Outline each Plasmodium vivax-infected red blood cell.
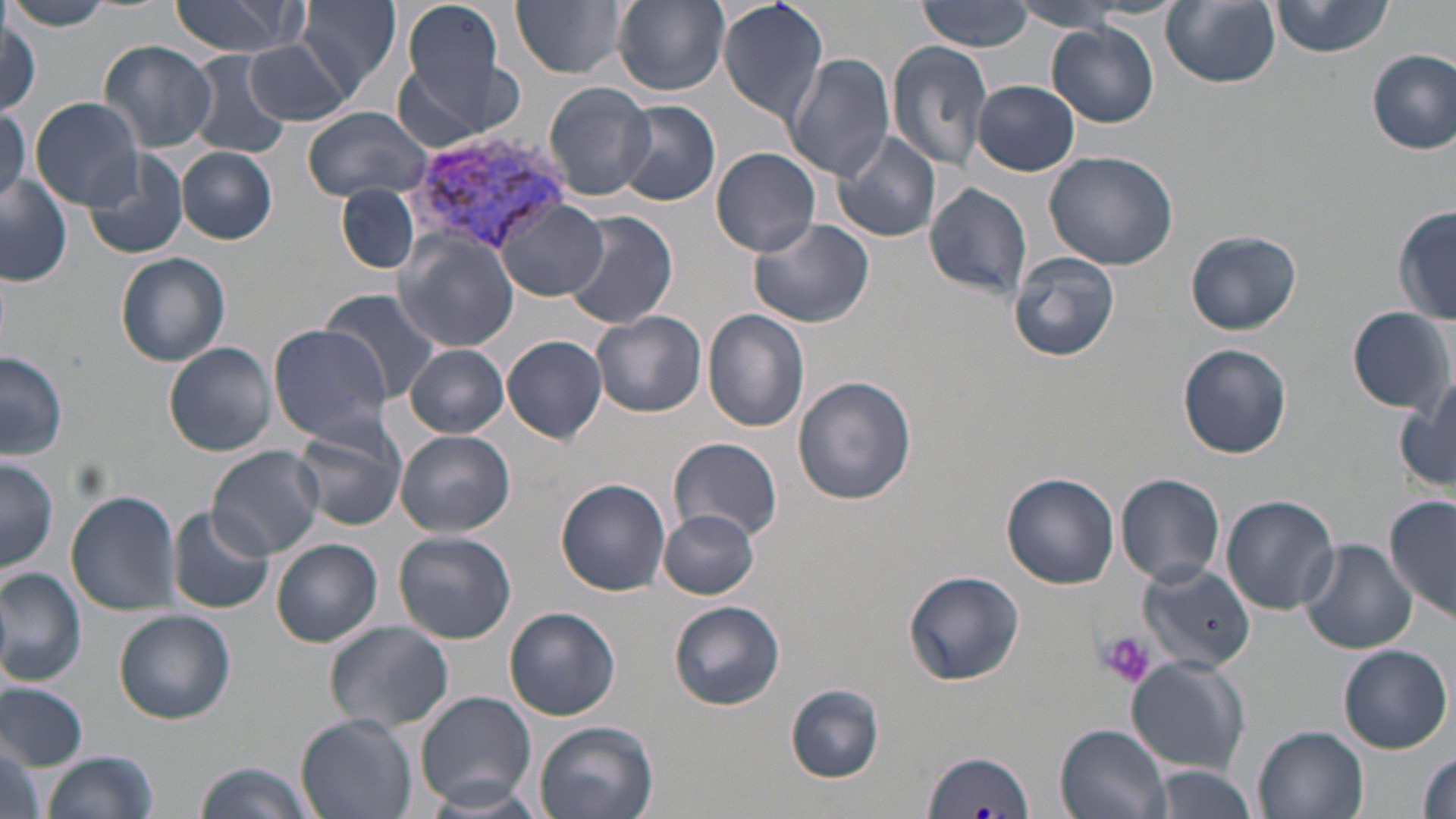

Approximate bounding boxes as (x1, y1, x2, y2) in pixels.
Plasmodium vivax-infected red blood cells: (405, 132, 571, 253).

slide-level diagnosis = Plasmodium vivax
stain = May-Grünwald-Giemsa
uninfected red blood cell locations = approximate bounding boxes as (x1, y1, x2, y2) in pixels: (163, 0, 304, 58), (296, 0, 402, 97), (400, 0, 509, 109), (511, 0, 630, 79), (614, 0, 730, 93), (716, 0, 830, 124), (918, 0, 1034, 52), (1270, 0, 1393, 57), (1162, 1, 1281, 88), (1, 3, 118, 32), (1008, 3, 1132, 36), (2, 15, 41, 116), (1048, 21, 1159, 127), (245, 39, 353, 126), (97, 40, 219, 153), (889, 41, 993, 170), (1368, 50, 1455, 153), (185, 51, 292, 159), (784, 53, 895, 182), (397, 62, 494, 153), (972, 80, 1080, 175), (545, 82, 656, 202), (30, 98, 147, 210), (615, 102, 720, 207), (0, 107, 28, 208), (302, 107, 435, 202), (831, 132, 943, 245), (177, 147, 277, 244), (712, 148, 822, 257), (83, 149, 190, 259), (1044, 151, 1177, 270), (0, 173, 74, 286), (924, 180, 1031, 301), (337, 184, 420, 274), (496, 200, 607, 301), (1394, 207, 1455, 324), (563, 210, 679, 330), (746, 217, 875, 328), (1184, 229, 1302, 335), (392, 231, 521, 353), (1009, 251, 1121, 361), (116, 253, 230, 366), (343, 263, 507, 394), (321, 289, 444, 403), (1348, 305, 1453, 414), (703, 309, 810, 432), (591, 310, 706, 418), (267, 324, 397, 444), (502, 334, 610, 444), (164, 341, 278, 457), (1178, 342, 1291, 458), (405, 345, 509, 437), (0, 349, 69, 460), (794, 376, 918, 506), (1397, 379, 1455, 494), (292, 418, 407, 530), (397, 431, 515, 536), (669, 437, 783, 543), (207, 447, 324, 561), (1, 456, 59, 571), (1001, 473, 1119, 589), (1115, 473, 1225, 585), (556, 479, 671, 595), (66, 490, 182, 614), (1385, 494, 1455, 623), (1220, 495, 1340, 614), (167, 506, 276, 615), (658, 510, 762, 600), (394, 531, 517, 644), (272, 539, 384, 648), (1300, 539, 1417, 656), (1139, 563, 1255, 673), (0, 568, 87, 686), (904, 572, 1024, 686), (668, 601, 784, 711), (505, 607, 620, 721), (115, 609, 236, 723), (324, 620, 455, 734), (1338, 645, 1451, 754), (1127, 657, 1249, 773), (0, 681, 87, 769), (785, 683, 884, 782), (416, 690, 537, 808), (297, 714, 417, 819), (532, 720, 658, 819), (1054, 724, 1174, 819), (1254, 726, 1368, 819), (1, 739, 49, 819), (921, 748, 1034, 818), (40, 750, 159, 819), (1415, 751, 1456, 819), (194, 761, 317, 819), (1145, 764, 1262, 819), (420, 781, 551, 818)
image size = 1456×819 pixels
field of view = single
modality = light microscopy
magnification = 1000x
platelet locations = approximate bounding boxes as (x1, y1, x2, y2) in pixels: (1096, 630, 1155, 690)
preparation = thin blood smear